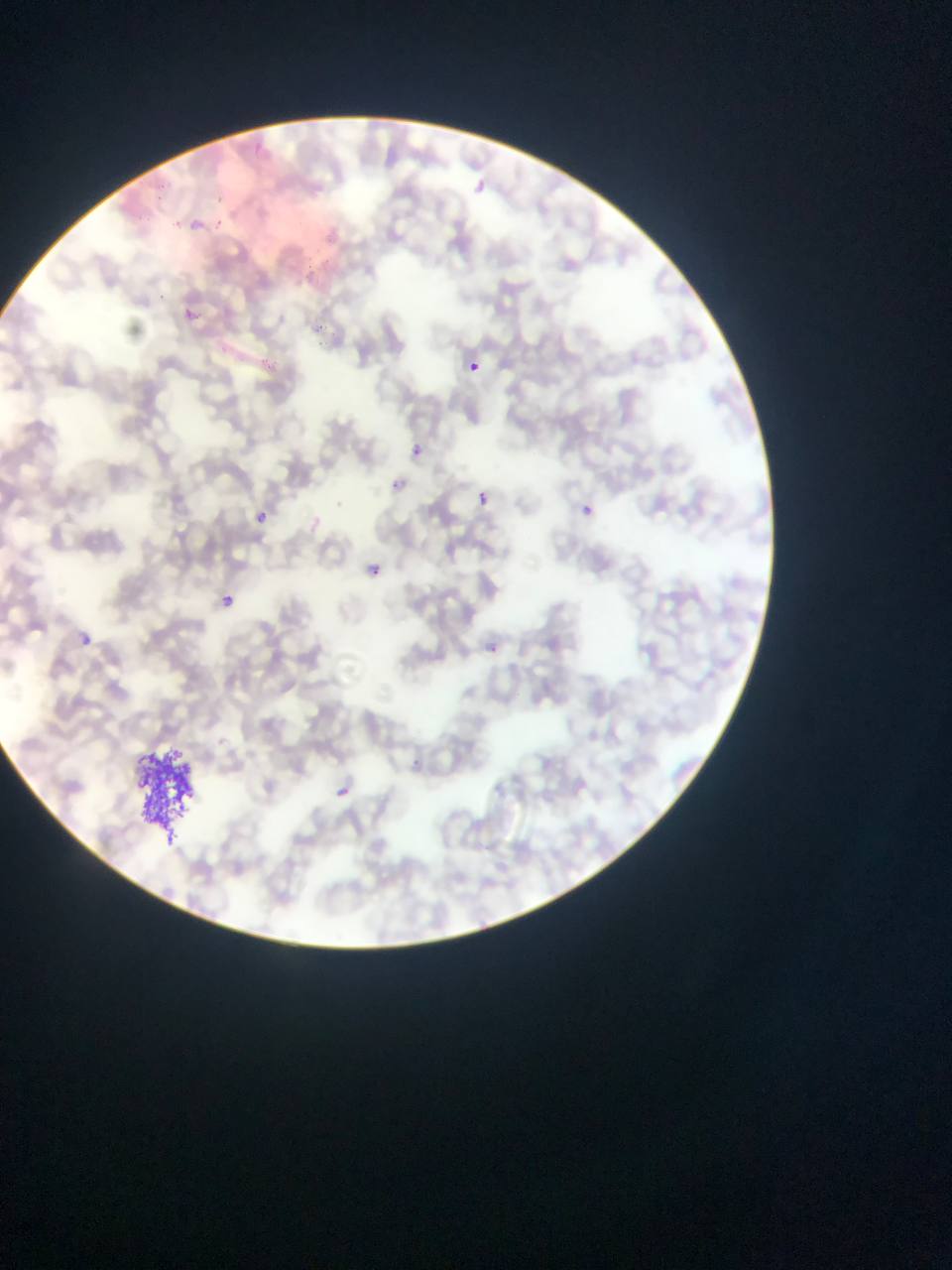

{
  "preparation": "thin blood smear",
  "artifact_stain_precipitate_or_debris_locations": "approximate bounding boxes as left top right bottom in pixels: 130 747 207 851",
  "country": "Ghana",
  "image_size": "952×1270 pixels",
  "field_of_view": "single",
  "capture": "mobile-phone photograph through a microscope",
  "plasmodium_parasite_locations": "approximate bounding boxes as left top right bottom in pixels: 253 141 275 159; 157 178 170 190; 154 192 175 208; 214 193 230 200; 192 218 210 235; 217 218 228 226; 186 304 193 315; 313 322 326 334; 315 341 335 349; 466 361 480 375; 409 444 424 459; 387 477 405 494; 474 489 491 507; 575 498 599 520; 249 506 272 528; 359 559 384 582; 220 594 235 608; 69 627 99 653; 477 638 507 664; 411 749 424 768; 333 782 355 802"
}